Locate and identify every blood parasite.
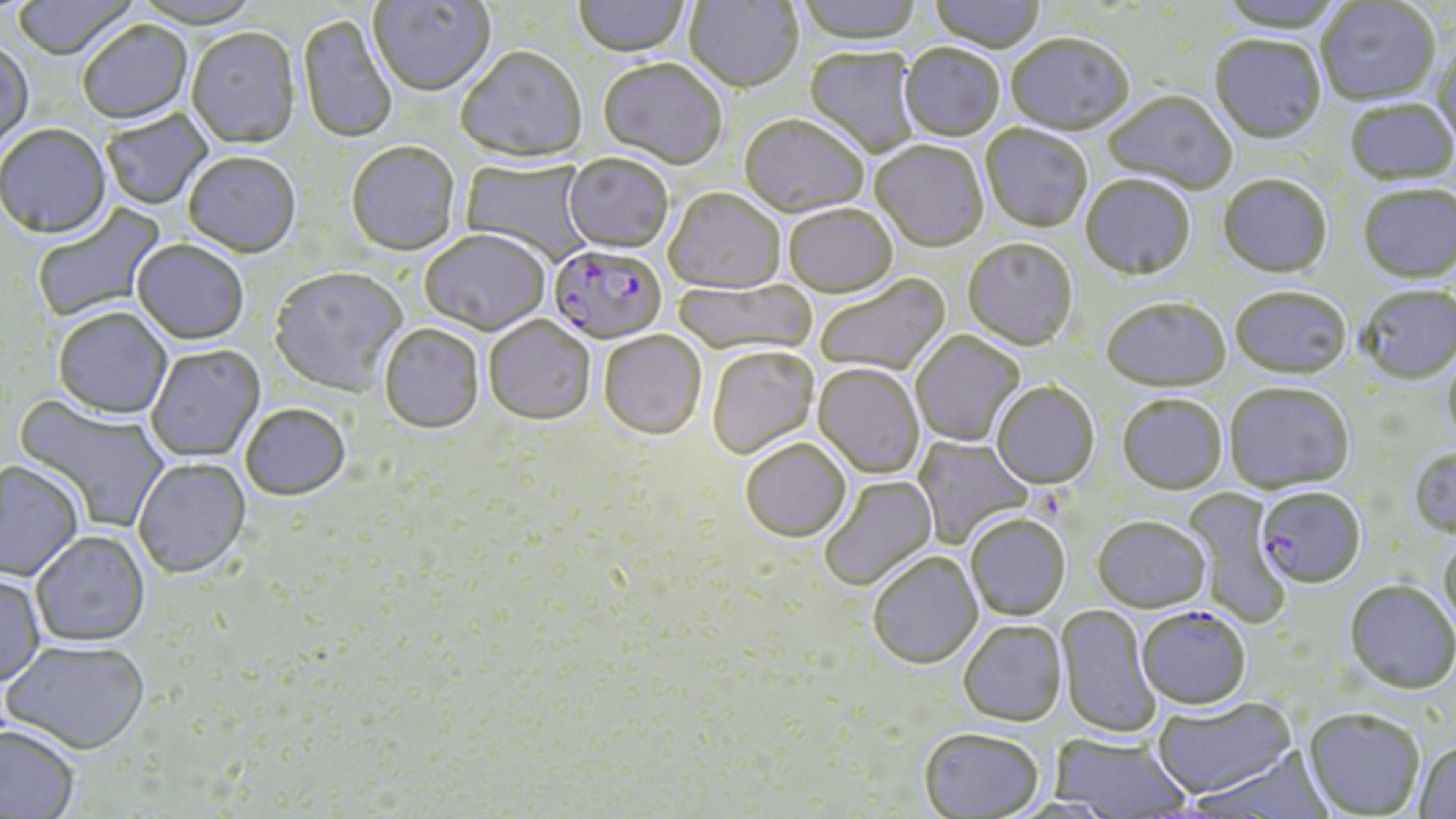
Approximate bounding boxes as (x1,y1)-(x2,y2) corner pairs in pixels.
Plasmodium falciparum-infected red blood cells: (547,246)-(667,347), (1256,489)-(1366,591), (1137,609)-(1251,713).
No Plasmodium ovale, Plasmodium malariae, Plasmodium vivax, Babesia divergens, or Trypanosoma brucei observed.

{
  "slide_level_diagnosis": "Plasmodium falciparum",
  "modality": "optical microscopy",
  "stain": "May-Grünwald-Giemsa",
  "magnification": "1000x",
  "preparation": "thin blood smear",
  "field_of_view": "one of a larger specimen",
  "image_size": "1456×819 pixels",
  "uninfected_red_blood_cell_locations": "approximate bounding boxes as (x1,y1)-(x2,y2) corner pairs in pixels: (12,0)-(137,63), (130,0)-(263,31), (369,0)-(496,99), (573,0)-(691,59), (684,0)-(803,95), (795,0)-(923,47), (928,0)-(1046,55), (1214,0)-(1347,35), (1317,1)-(1441,109), (297,14)-(397,146), (78,22)-(193,127), (186,30)-(300,151), (1006,36)-(1133,138), (1209,38)-(1326,147), (0,44)-(34,154), (899,46)-(1004,143), (1431,46)-(1456,157), (456,49)-(587,166), (804,49)-(921,158), (597,60)-(726,172), (1103,93)-(1237,196), (1345,100)-(1456,188), (101,110)-(214,210), (739,116)-(869,220), (980,126)-(1092,234), (0,127)-(112,242), (870,143)-(988,254), (346,144)-(461,258), (183,155)-(301,260), (564,155)-(673,256), (460,159)-(594,264), (1218,176)-(1333,281), (1080,177)-(1195,283), (1358,186)-(1456,287), (664,191)-(785,296), (32,200)-(169,323), (784,207)-(898,300), (420,233)-(551,338), (962,240)-(1078,353), (131,242)-(248,347), (268,269)-(408,399), (815,275)-(951,377), (672,280)-(817,359), (1358,288)-(1456,385), (1230,290)-(1352,383), (1101,300)-(1231,394), (52,309)-(173,422), (483,318)-(595,428), (379,325)-(484,436), (911,331)-(1026,447), (599,333)-(706,442), (147,345)-(266,463), (1441,345)-(1456,451), (707,348)-(819,461), (812,365)-(925,481), (992,384)-(1099,491), (1224,385)-(1354,496), (14,395)-(171,534), (1117,397)-(1227,497), (240,406)-(351,504), (913,435)-(1033,547), (741,442)-(851,545), (1407,449)-(1456,540), (133,458)-(252,581), (0,462)-(83,583), (820,476)-(939,593), (1182,489)-(1292,629), (965,516)-(1070,622), (1093,518)-(1210,616), (30,531)-(150,648), (1438,537)-(1456,636), (868,553)-(983,671), (0,574)-(46,690), (1344,582)-(1456,697), (1055,604)-(1160,739), (958,622)-(1068,729), (2,641)-(150,757), (1152,699)-(1297,802), (1302,711)-(1425,818), (0,725)-(80,819), (919,731)-(1043,818), (1048,734)-(1191,818), (1413,739)-(1456,819), (1190,748)-(1334,819)"
}